Locate every Plasmodium falciparum-infected red blood cell.
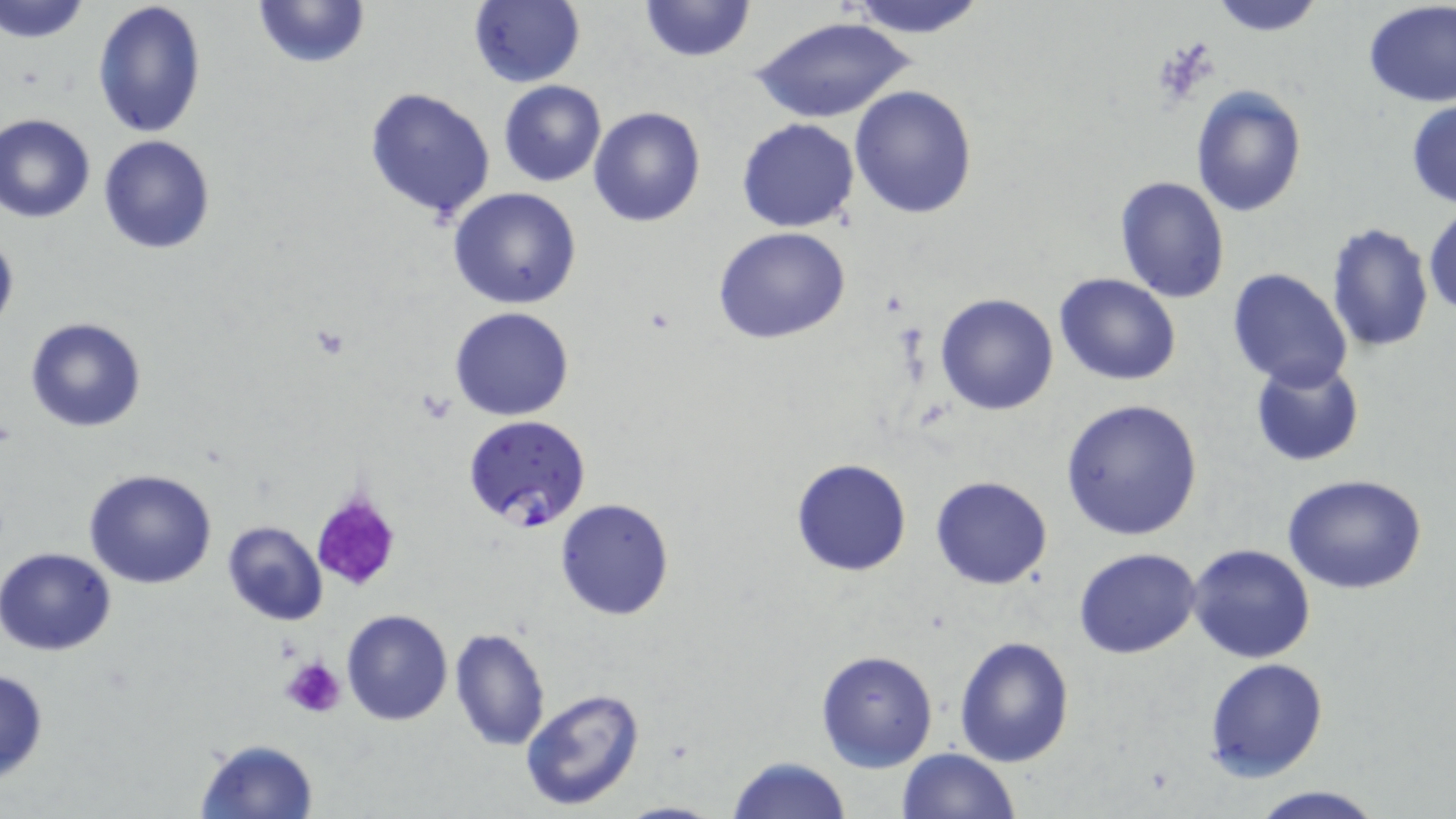
Approximate bounding boxes as named x1/y1/x2/y2 corners in pixels.
Plasmodium falciparum-infected red blood cells: (x1=464, y1=415, x2=593, y2=533).

Summary:
  - Platelet locations: (x1=307, y1=490, x2=404, y2=593), (x1=282, y1=657, x2=345, y2=719)
  - Uninfected red blood cell locations: (x1=2, y1=0, x2=93, y2=43), (x1=93, y1=0, x2=209, y2=142), (x1=250, y1=0, x2=370, y2=70), (x1=636, y1=0, x2=757, y2=65), (x1=844, y1=0, x2=988, y2=40), (x1=1205, y1=0, x2=1331, y2=35), (x1=1361, y1=1, x2=1455, y2=107), (x1=466, y1=2, x2=586, y2=88), (x1=750, y1=14, x2=914, y2=125), (x1=497, y1=80, x2=606, y2=187), (x1=848, y1=84, x2=978, y2=218), (x1=1190, y1=86, x2=1307, y2=216), (x1=364, y1=87, x2=496, y2=222), (x1=1406, y1=100, x2=1456, y2=209), (x1=588, y1=106, x2=705, y2=227), (x1=1, y1=114, x2=96, y2=224), (x1=736, y1=118, x2=861, y2=233), (x1=98, y1=135, x2=217, y2=255), (x1=1115, y1=176, x2=1230, y2=303), (x1=447, y1=187, x2=582, y2=311), (x1=1424, y1=206, x2=1456, y2=319), (x1=1325, y1=222, x2=1433, y2=354), (x1=0, y1=226, x2=18, y2=339), (x1=714, y1=228, x2=852, y2=346), (x1=1227, y1=269, x2=1352, y2=390), (x1=1054, y1=272, x2=1182, y2=386), (x1=935, y1=293, x2=1058, y2=415), (x1=450, y1=308, x2=575, y2=421), (x1=25, y1=317, x2=147, y2=433), (x1=1249, y1=361, x2=1364, y2=467), (x1=1059, y1=398, x2=1205, y2=542), (x1=790, y1=458, x2=913, y2=577), (x1=83, y1=468, x2=219, y2=589), (x1=1282, y1=474, x2=1429, y2=593), (x1=930, y1=476, x2=1053, y2=589), (x1=554, y1=498, x2=675, y2=621), (x1=222, y1=520, x2=329, y2=626), (x1=1186, y1=544, x2=1315, y2=664), (x1=1072, y1=545, x2=1201, y2=658), (x1=0, y1=546, x2=119, y2=655), (x1=340, y1=610, x2=454, y2=727), (x1=447, y1=626, x2=551, y2=751), (x1=953, y1=635, x2=1074, y2=767), (x1=815, y1=648, x2=939, y2=772), (x1=1205, y1=658, x2=1329, y2=782), (x1=0, y1=666, x2=48, y2=785), (x1=519, y1=687, x2=646, y2=812), (x1=193, y1=737, x2=320, y2=819), (x1=897, y1=747, x2=1020, y2=819), (x1=725, y1=756, x2=853, y2=818), (x1=1244, y1=783, x2=1386, y2=818), (x1=612, y1=799, x2=728, y2=819)
  - Slide-level diagnosis: Plasmodium falciparum
  - Image size: 1456×819 pixels
  - Stain: May-Grünwald-Giemsa
  - Field of view: single
  - Magnification: 1000x
  - Preparation: thin blood film
  - Modality: light microscopy